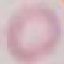

{
  "malaria_status": "uninfected",
  "stain": "Giemsa",
  "capture": "smartphone camera at the microscope eyepiece",
  "preparation": "thin blood film",
  "image_type": "automatically extracted cell patch, resized to 64 × 64 pixels"
}